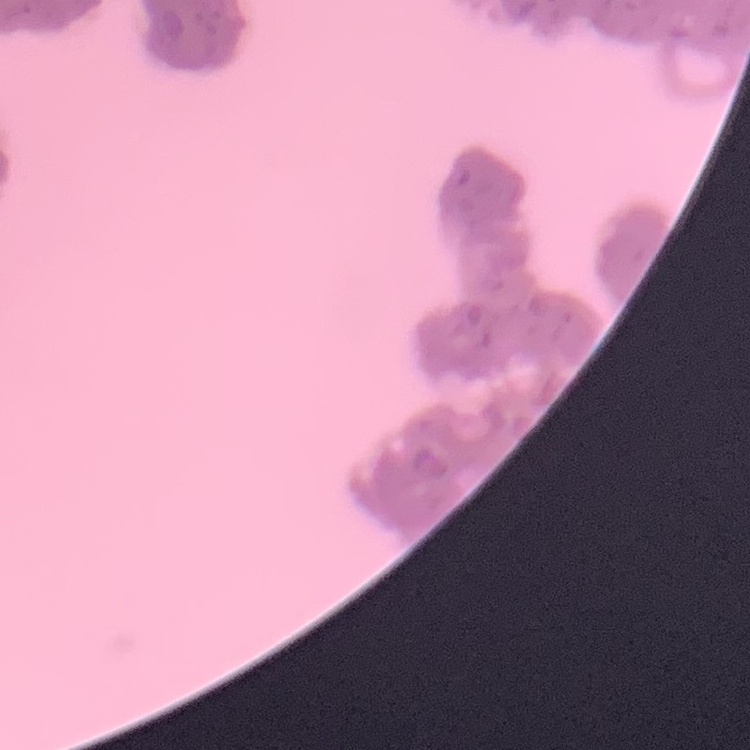 The red blood cells show rouleaux formation. One tile cut from a larger photomicrograph. Stained with either Field's or Giemsa. Thin blood smear.